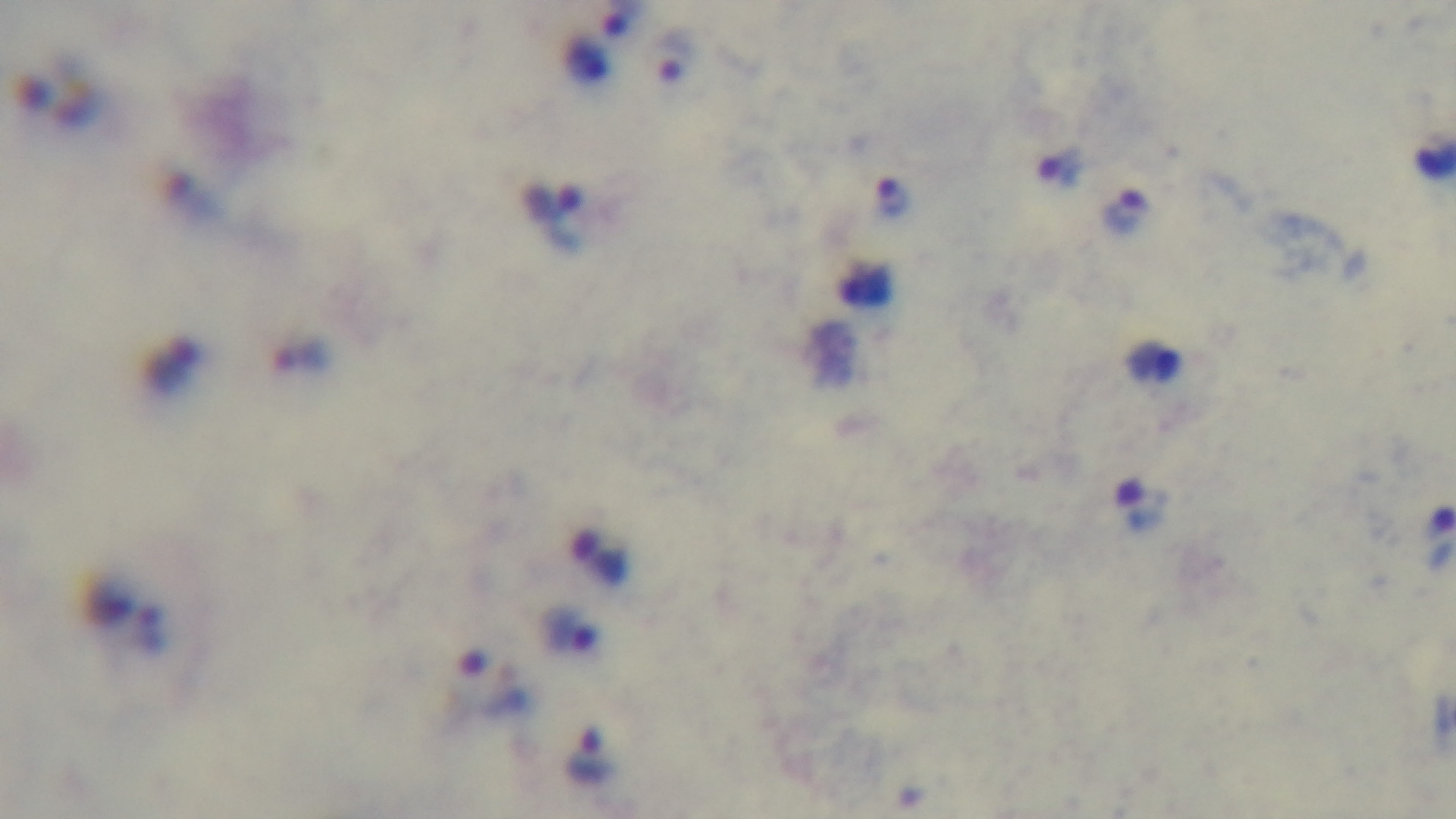 Preparation: thick smear. Light microscopy. Captured with a mounted 4K digital camera. Oil-immersion objective, 100x. One field from the slide. Malaria status: infected. Giemsa stain.